Outline each blood parasite and name the species.
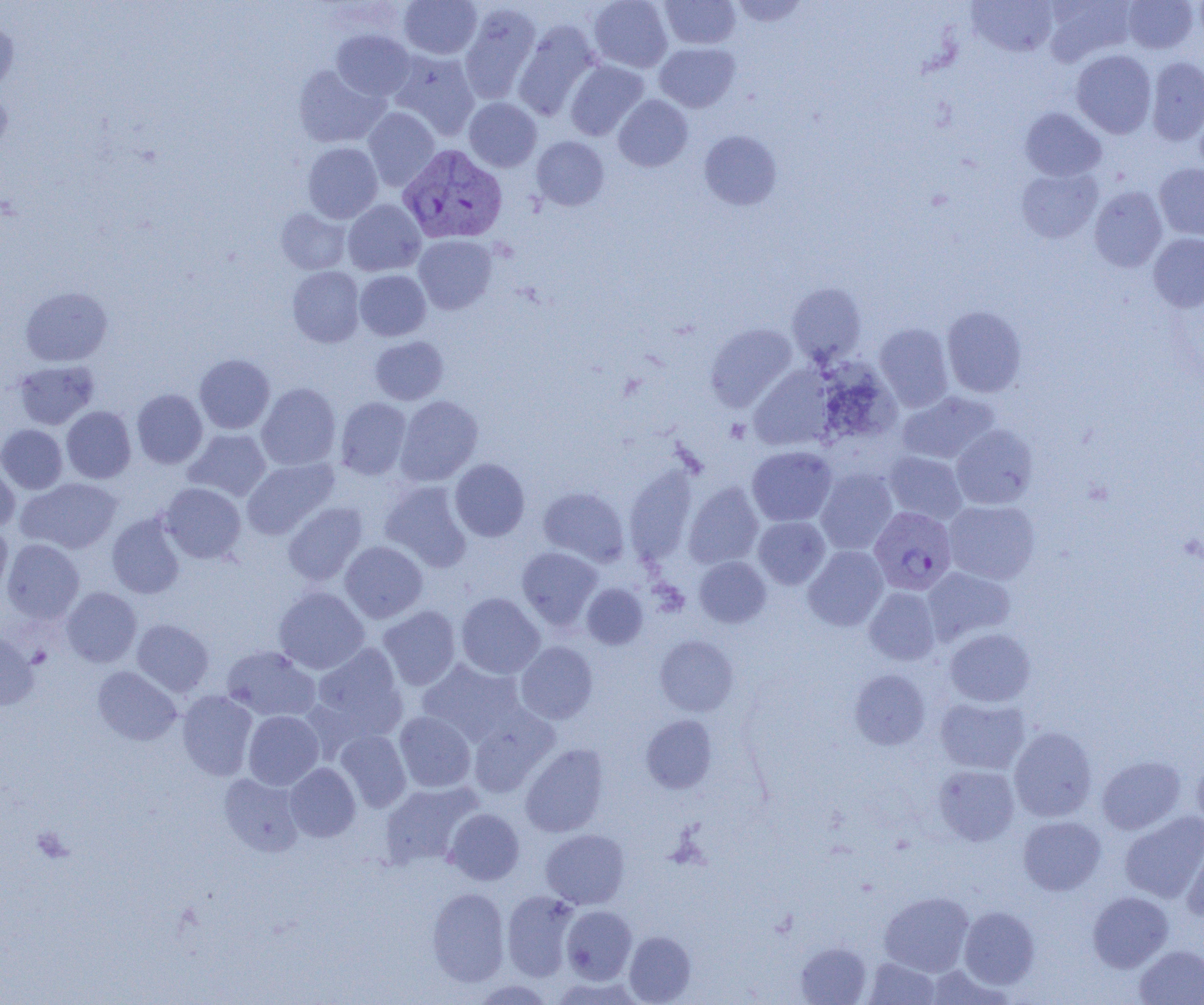

Approximate bounding boxes as (x1,y1)-(x2,y2) corner pairs in pixels.
Plasmodium vivax-infected red blood cells: (398,144)-(507,244), (869,506)-(957,595).
No Plasmodium falciparum, Plasmodium ovale, Plasmodium malariae, Babesia divergens, or Trypanosoma brucei observed.

Uninfected red blood cell locations: (399,0)-(482,59), (589,0)-(672,72), (660,0)-(740,49), (730,0)-(808,27), (1042,0)-(1136,66), (1123,0)-(1199,53), (967,1)-(1059,57), (459,4)-(541,103), (0,16)-(18,92), (513,21)-(600,120), (331,29)-(414,100), (655,42)-(740,112), (388,50)-(480,139), (1071,50)-(1157,138), (1145,56)-(1204,145), (565,60)-(648,140), (294,65)-(388,147), (0,87)-(11,158), (613,95)-(693,171), (464,98)-(541,172), (1019,107)-(1106,181), (363,108)-(440,190), (699,130)-(782,210), (532,136)-(609,210), (303,142)-(383,223), (1154,163)-(1204,242), (1017,167)-(1102,243), (1089,186)-(1168,272), (343,199)-(425,275), (276,207)-(351,274), (1148,233)-(1204,312), (414,235)-(497,314), (287,266)-(365,347), (355,270)-(431,340), (786,283)-(866,365), (20,287)-(112,366), (942,305)-(1027,397), (706,323)-(798,411), (874,323)-(954,412), (370,336)-(448,405), (194,354)-(275,433), (13,360)-(99,430), (818,362)-(901,445), (749,367)-(837,451), (257,383)-(341,470), (132,389)-(208,468), (897,391)-(999,465), (396,395)-(482,485), (335,397)-(411,480), (61,406)-(136,483), (0,424)-(68,494), (951,425)-(1038,510), (185,429)-(271,501), (747,446)-(837,526), (884,451)-(967,523), (242,458)-(338,539), (449,458)-(529,541), (0,460)-(20,531), (815,468)-(897,555), (16,477)-(122,554), (380,480)-(472,571), (160,482)-(246,563), (684,482)-(764,569), (538,486)-(629,566), (943,500)-(1040,584), (283,502)-(367,585), (107,513)-(186,599), (753,516)-(830,589), (0,521)-(12,599), (2,539)-(84,623), (340,541)-(428,623), (516,546)-(603,630), (803,546)-(888,631), (694,556)-(770,627), (922,566)-(1015,644), (582,583)-(648,649), (61,587)-(142,667), (273,587)-(369,674), (864,587)-(940,665), (455,592)-(544,679), (378,605)-(461,690), (131,619)-(214,697), (944,628)-(1036,707), (0,632)-(39,710), (655,635)-(739,716), (515,641)-(598,724), (311,643)-(407,740), (222,645)-(320,721), (415,659)-(526,746), (93,666)-(182,746), (850,669)-(931,749), (177,690)-(258,780), (935,696)-(1030,774), (467,707)-(558,798), (243,711)-(324,789), (394,711)-(476,792), (641,714)-(717,793), (1009,727)-(1097,822), (334,730)-(411,812), (520,744)-(609,837), (1096,755)-(1186,834), (1192,758)-(1204,831), (285,763)-(360,842), (934,764)-(1020,845), (219,773)-(305,857), (380,781)-(481,867), (444,808)-(524,885), (1120,811)-(1204,903), (1018,815)-(1106,895), (540,829)-(630,909), (1182,834)-(1204,922), (427,888)-(510,986), (502,890)-(580,981), (879,891)-(974,976), (1088,891)-(1173,972), (561,905)-(637,984), (958,906)-(1040,989), (624,931)-(696,1004), (794,941)-(872,1004), (1134,945)-(1204,1005), (863,957)-(940,1004), (471,979)-(555,1004). Slide-level diagnosis: Plasmodium vivax. Optical microscopy. Single field of view. Thin blood smear. Captured at 1000x magnification. Image is 1204×1005 pixels.